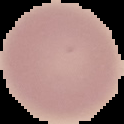
Summary:
  - Image size: 124×124 pixels
  - Preparation: thin blood film
  - Image type: segmented cell region with the area outside set to black
  - Malaria status: uninfected